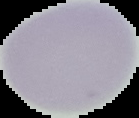
The area outside the segmented cell region is set to black. Image is 139×118 pixels. From a thin blood film. Malaria status: uninfected.